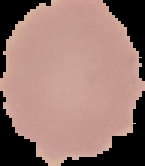 Result: negative for malaria parasites. Image is 145×166 pixels. From a thin blood smear. Cell region segmented out of the field of view; the surrounding area is masked to black.